Locate every parasitized red blood cell.
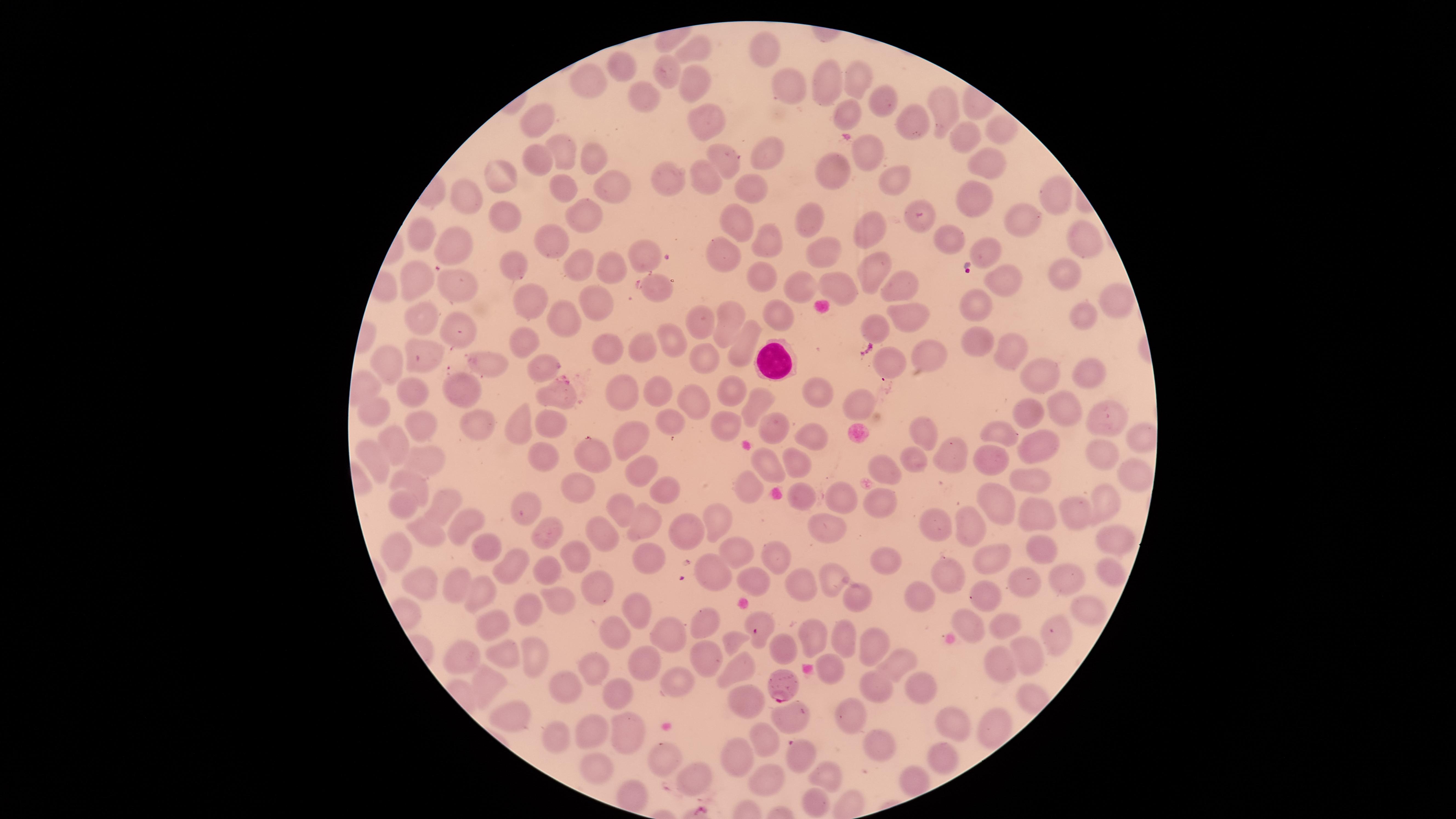

Approximate marker points as {x, y} in pixels.
Parasitized red blood cells: {785, 684}.

Approximate marker points as {x, y} in pixels. Uninfected red blood cells: {693, 46}, {763, 49}, {624, 62}, {666, 71}, {857, 76}, {699, 79}, {823, 81}, {591, 82}, {788, 85}, {645, 99}, {886, 103}, {943, 104}, {843, 111}, {541, 119}, {705, 120}, {908, 120}, {1000, 129}, {962, 136}, {561, 151}, {871, 152}, {768, 154}, {598, 159}, {540, 160}, {723, 161}, {983, 165}, {833, 171}, {499, 172}, {669, 174}, {893, 175}, {706, 179}, {607, 180}, {563, 184}, {748, 185}, {976, 195}, {1051, 198}, {466, 199}, {585, 212}, {504, 216}, {920, 220}, {1015, 220}, {809, 221}, {733, 224}, {874, 228}, {424, 234}, {943, 234}, {552, 238}, {1077, 240}, {760, 241}, {455, 245}, {986, 246}, {825, 251}, {722, 252}, {637, 255}, {514, 262}, {582, 266}, {610, 266}, {873, 267}, {1067, 272}, {413, 275}, {758, 276}, {1009, 282}, {454, 283}, {801, 287}, {842, 287}, {899, 287}, {1110, 296}, {527, 298}, {597, 303}, {978, 306}, {778, 313}, {424, 314}, {728, 314}, {558, 315}, {1078, 315}, {907, 318}, {700, 321}, {870, 327}, {461, 331}, {524, 337}, {978, 339}, {670, 341}, {743, 343}, {1004, 346}, {645, 348}, {606, 350}, {921, 354}, {420, 355}, {700, 360}, {493, 361}, {391, 362}, {891, 363}, {540, 365}, {1085, 373}, {1042, 375}, {736, 386}, {816, 387}, {458, 388}, {620, 390}, {655, 390}, {416, 394}, {554, 394}, {689, 399}, {858, 402}, {758, 403}, {380, 405}, {1063, 410}, {1028, 413}, {1112, 416}, {518, 420}, {547, 421}, {724, 421}, {479, 422}, {678, 422}, {771, 424}, {923, 431}, {995, 431}, {423, 432}, {806, 432}, {625, 437}, {398, 446}, {1036, 446}, {1101, 453}, {590, 456}, {429, 457}, {542, 457}, {954, 457}, {374, 459}, {794, 460}, {989, 461}, {910, 462}, {768, 465}, {881, 465}, {639, 467}, {1137, 473}, {407, 476}, {1031, 478}, {750, 483}, {667, 484}, {576, 486}, {1102, 494}, {801, 496}, {840, 499}, {405, 500}, {446, 503}, {998, 503}, {524, 504}, {623, 504}, {1078, 511}, {880, 512}, {1039, 519}, {719, 520}, {461, 521}, {636, 521}, {933, 521}, {822, 525}, {969, 526}, {678, 530}, {426, 532}, {547, 532}, {599, 532}, {1108, 535}, {736, 549}, {1041, 549}, {400, 554}, {778, 554}, {572, 555}, {651, 555}, {986, 557}, {880, 559}, {547, 564}, {514, 566}, {714, 570}, {1103, 573}, {945, 574}, {837, 577}, {1065, 577}, {750, 579}, {798, 584}, {1025, 584}, {428, 585}, {589, 585}, {481, 591}, {990, 591}, {921, 595}, {456, 596}, {557, 599}, {856, 599}, {1093, 608}, {528, 609}, {641, 613}, {761, 617}, {1000, 618}, {968, 619}, {707, 620}, {498, 628}, {614, 631}, {668, 634}, {813, 635}, {1056, 636}, {733, 638}, {841, 638}, {873, 643}, {779, 650}, {1028, 651}, {459, 654}, {531, 654}, {504, 657}, {711, 660}, {1000, 663}, {650, 664}, {897, 666}, {737, 667}, {830, 667}, {597, 668}, {563, 682}, {676, 683}, {486, 684}, {879, 686}, {926, 690}, {613, 693}, {742, 701}, {790, 711}, {508, 714}, {853, 714}, {958, 719}, {994, 723}, {588, 729}, {630, 732}, {558, 735}, {772, 739}, {881, 751}, {941, 755}, {669, 756}, {732, 759}, {801, 761}, {598, 767}, {834, 774}, {696, 775}, {914, 778}, {768, 779}, {812, 802}. White blood cells: {772, 359}. Giemsa-stained preparation. Image is 1456×819 pixels. Species: Plasmodium falciparum. Single field of view. Thin blood smear. Circular visible region. Smartphone photograph through the microscope eyepiece.